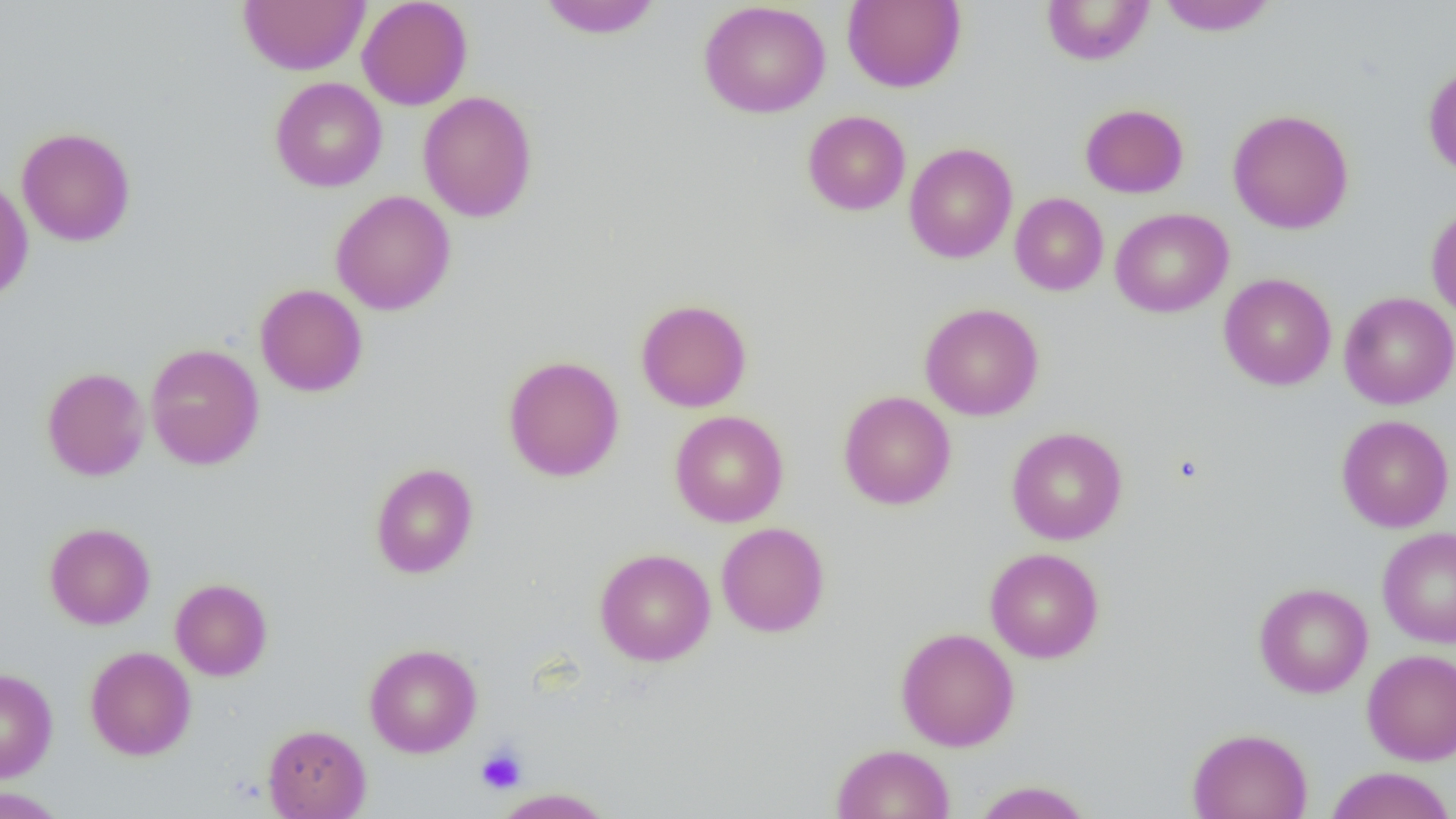
slide-level diagnosis = no evidence of blood parasites
platelet locations = approximate bounding boxes as [x1, y1, x2, y2] in pixels: [476, 746, 526, 794]
uninfected red blood cell locations = approximate bounding boxes as [x1, y1, x2, y2] in pixels: [238, 0, 369, 75], [357, 0, 473, 110], [536, 0, 663, 38], [699, 0, 831, 119], [842, 0, 965, 92], [1157, 0, 1278, 36], [1040, 1, 1155, 65], [1423, 63, 1456, 178], [270, 77, 387, 192], [418, 91, 538, 223], [1080, 103, 1189, 198], [1228, 108, 1354, 234], [803, 110, 911, 215], [16, 127, 136, 247], [904, 142, 1017, 263], [0, 177, 33, 304], [330, 190, 456, 315], [1010, 193, 1108, 295], [1426, 203, 1456, 322], [1110, 208, 1233, 317], [1218, 273, 1336, 390], [254, 283, 368, 397], [1339, 291, 1456, 409], [635, 298, 752, 412], [919, 302, 1044, 421], [145, 343, 264, 470], [503, 355, 625, 481], [42, 367, 150, 481], [838, 391, 956, 510], [669, 410, 788, 527], [1336, 414, 1454, 533], [1006, 427, 1127, 544], [370, 462, 479, 578], [44, 522, 155, 629], [716, 522, 830, 637], [1377, 526, 1456, 648], [985, 547, 1104, 663], [594, 548, 716, 666], [170, 578, 272, 681], [1254, 582, 1373, 698], [895, 627, 1019, 751], [363, 643, 482, 757], [84, 646, 196, 760], [1362, 649, 1456, 765], [0, 668, 58, 782], [263, 724, 371, 819], [1187, 728, 1312, 819], [831, 743, 955, 819], [1324, 767, 1455, 819], [972, 780, 1094, 819], [0, 787, 68, 819], [493, 787, 612, 818]
image size = 1456×819 pixels
modality = optical microscopy
field of view = single
preparation = thin blood film
magnification = 1000x